Assess this cell for malaria.
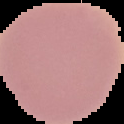
Uninfected.

Summary:
  - Image size: 124×124 pixels
  - Preparation: thin blood film
  - Image type: segmented cell region on a black background